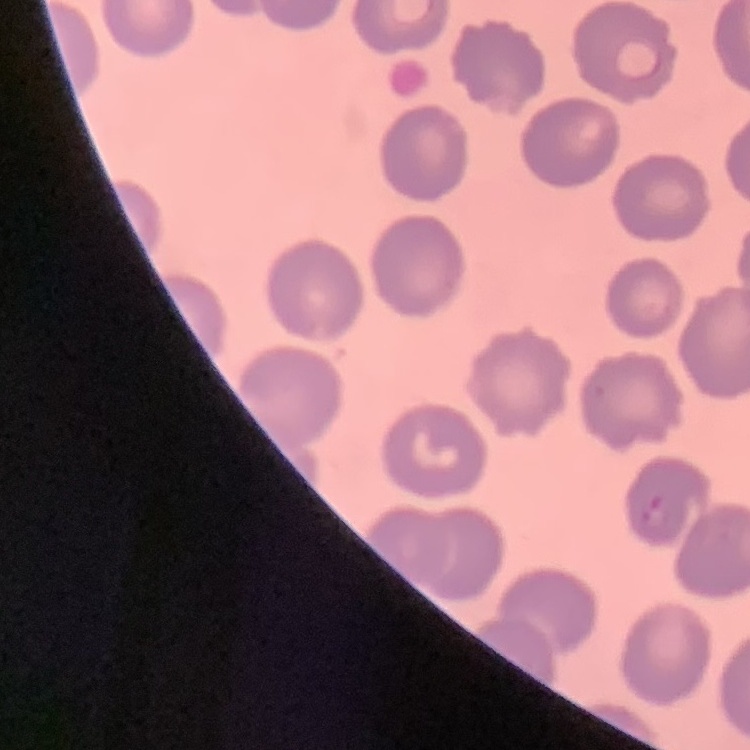

The red blood cells show no rouleaux formation. Thin blood smear. Field's or Giemsa stain. Square crop of a larger photomicrograph.